Identify the blood parasite species.
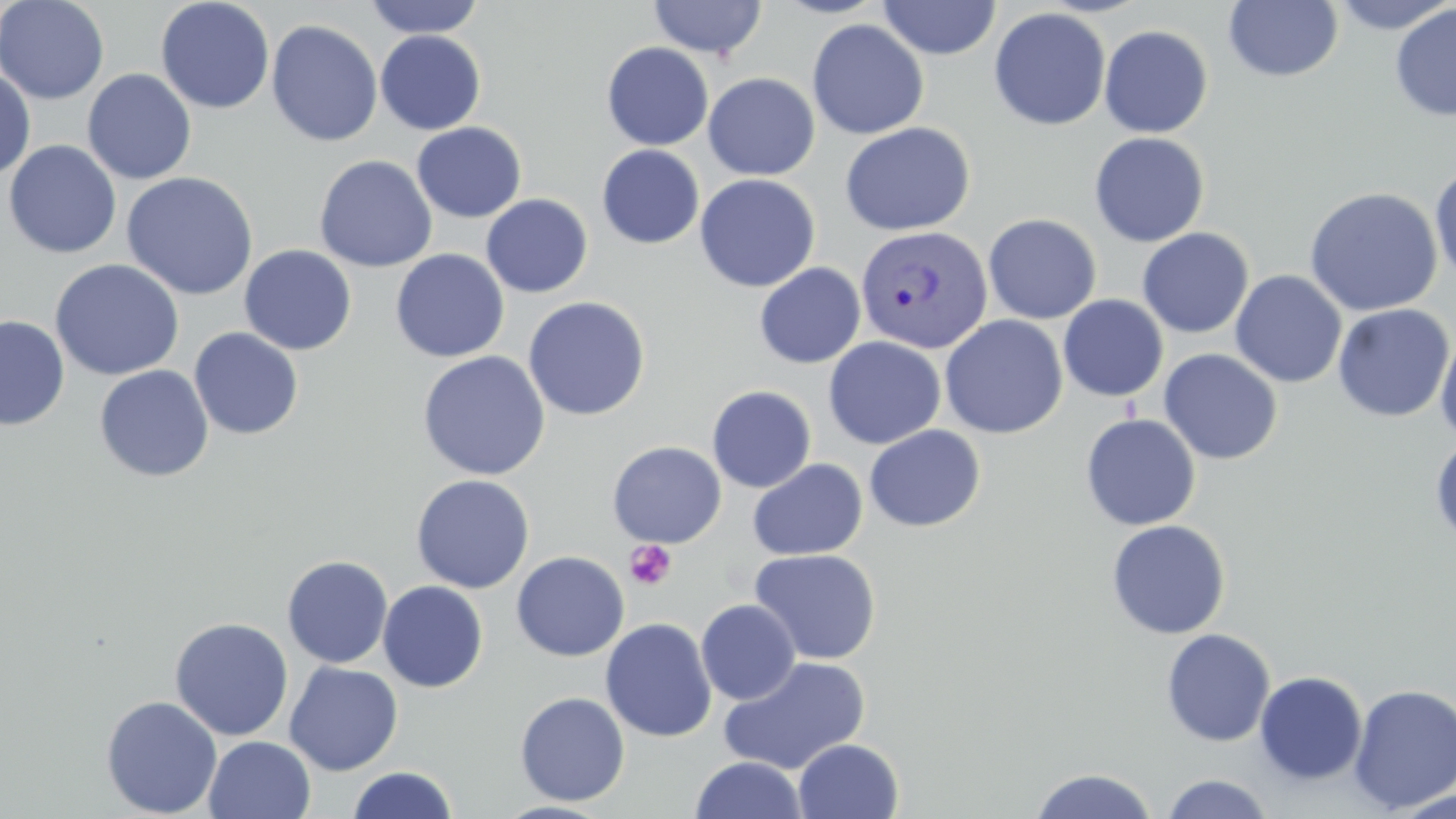
Plasmodium vivax.

Summary:
  - Coordinate format: approximate bounding boxes as [x1, y1, x2, y2] in pixels
  - Uninfected red blood cell locations: [0, 0, 109, 104], [155, 0, 275, 114], [363, 0, 486, 39], [648, 0, 767, 60], [772, 0, 890, 19], [1324, 0, 1456, 35], [877, 1, 1001, 61], [1223, 1, 1344, 82], [1389, 3, 1456, 122], [989, 7, 1111, 131], [266, 19, 383, 147], [807, 19, 929, 140], [1099, 25, 1213, 138], [375, 30, 486, 135], [602, 42, 714, 151], [0, 68, 36, 179], [82, 68, 197, 185], [702, 72, 820, 180], [411, 122, 527, 222], [839, 122, 975, 236], [1089, 132, 1210, 247], [3, 139, 122, 259], [597, 145, 705, 249], [314, 154, 438, 272], [1429, 164, 1456, 286], [120, 171, 259, 301], [694, 173, 821, 292], [1304, 186, 1443, 317], [481, 194, 593, 298], [983, 213, 1102, 324], [1137, 227, 1254, 338], [239, 244, 356, 355], [390, 249, 510, 362], [49, 259, 185, 380], [754, 262, 865, 368], [1230, 270, 1347, 388], [1058, 295, 1169, 402], [523, 296, 650, 420], [1332, 303, 1454, 422], [0, 315, 70, 430], [939, 315, 1068, 439], [188, 327, 304, 440], [1435, 330, 1456, 446], [823, 337, 946, 449], [1158, 348, 1283, 465], [417, 350, 551, 481], [94, 364, 214, 482], [707, 385, 816, 492], [1080, 413, 1201, 531], [864, 425, 986, 532], [1430, 436, 1456, 547], [607, 441, 726, 548], [747, 459, 868, 561], [411, 474, 535, 594], [1106, 519, 1230, 640], [748, 549, 882, 664], [511, 551, 629, 661], [281, 555, 393, 668], [377, 581, 488, 693], [696, 599, 801, 704], [170, 617, 294, 741], [600, 617, 718, 743], [1160, 628, 1275, 747], [717, 655, 871, 775], [284, 661, 403, 776], [1254, 671, 1368, 785], [1348, 684, 1456, 812], [514, 691, 630, 806], [101, 695, 222, 818], [203, 735, 316, 819], [793, 738, 904, 819], [690, 755, 808, 818], [347, 766, 458, 819], [1029, 768, 1160, 818], [1160, 773, 1275, 819], [1388, 789, 1456, 818]
  - Plasmodium vivax-infected red blood cell locations: [855, 224, 992, 355]
  - Platelet locations: [624, 540, 677, 591]
  - Image size: 1456×819 pixels
  - Preparation: thin blood film
  - Field of view: single
  - Modality: optical microscopy
  - Magnification: 1000x
  - Stain: May-Grünwald-Giemsa